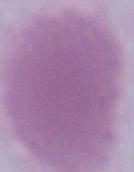

magnification = 1000x
identification = erythrocyte
modality = micrograph